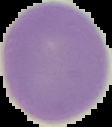
malaria status = uninfected
image type = segmented cell region with the area outside set to black
image size = 112×127 pixels
preparation = thin blood smear